Classify this cell by malaria status.
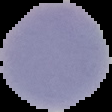

Uninfected.

Summary:
  - Image type: segmented cell region with the area outside set to black
  - Image size: 112×112 pixels
  - Preparation: thin blood film